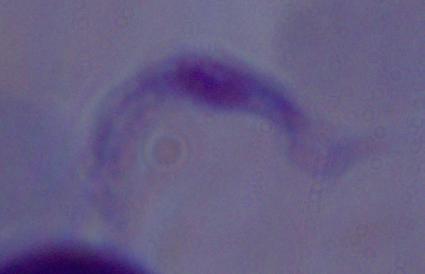

Summary:
  - Modality: micrograph
  - Magnification: 1000x
  - Identification: trypanosome